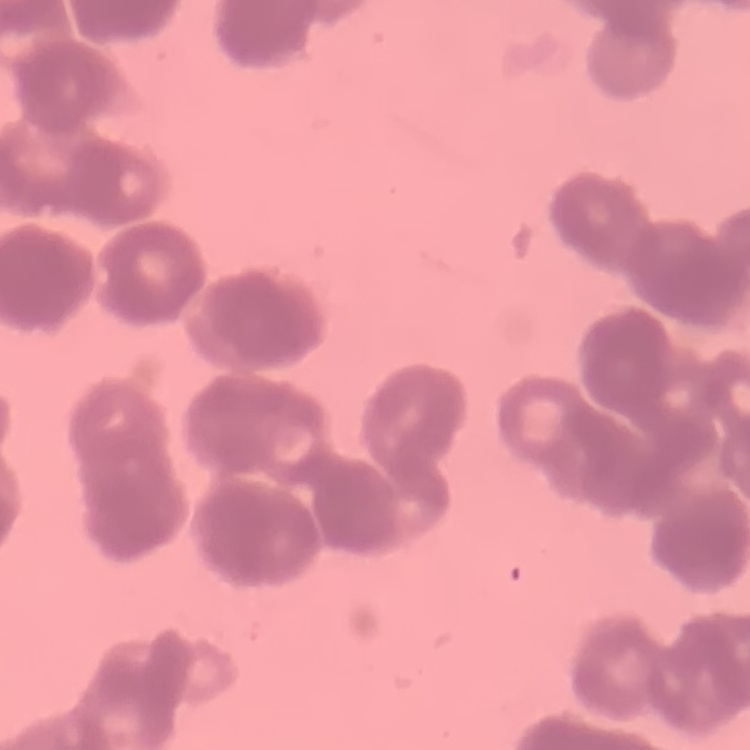
{
  "red_blood_cell_morphology": "rouleaux formation",
  "stain": "Field's or Giemsa",
  "image_type": "square crop of a larger photomicrograph",
  "preparation": "thin blood film"
}